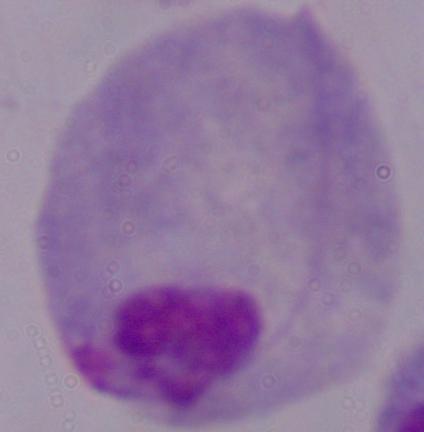

magnification = 1000x
identification = trichomonad
modality = photomicrograph